Evaluate for Plasmodium parasites.
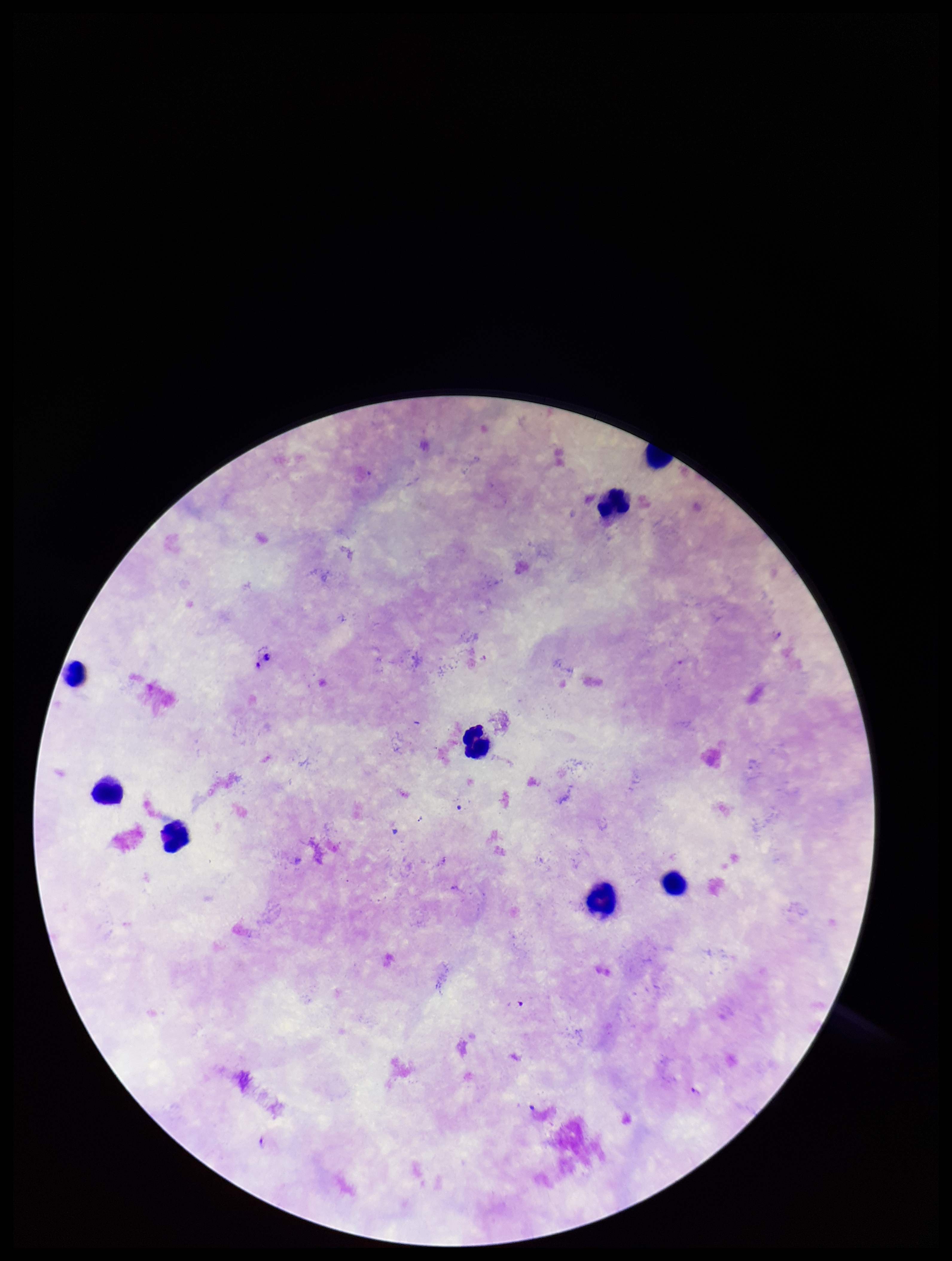

Seen.

Parasite count: 3. Preparation: thick smear. One field from this slide. Patient malaria status: infected. Leukocyte count: 8. Image is 952×1261 pixels. Giemsa stain. Photographed through the microscope eyepiece with a smartphone camera. Species reported for this patient: Plasmodium falciparum.